Assess this cell for malaria.
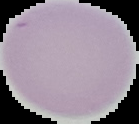
It is uninfected.

From a thin blood smear. Image is 139×124 pixels. The area outside the segmented cell region is set to black.